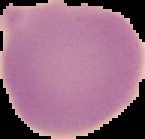

Summary:
  - Image type: cell region segmented out of the field of view; surrounding area masked to black
  - Result: negative for malaria parasites
  - Image size: 145×139 pixels
  - Preparation: thin blood film